State which parasite is depicted.
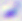
Toxoplasma gondii.

Photomicrograph. Captured at 400x magnification.